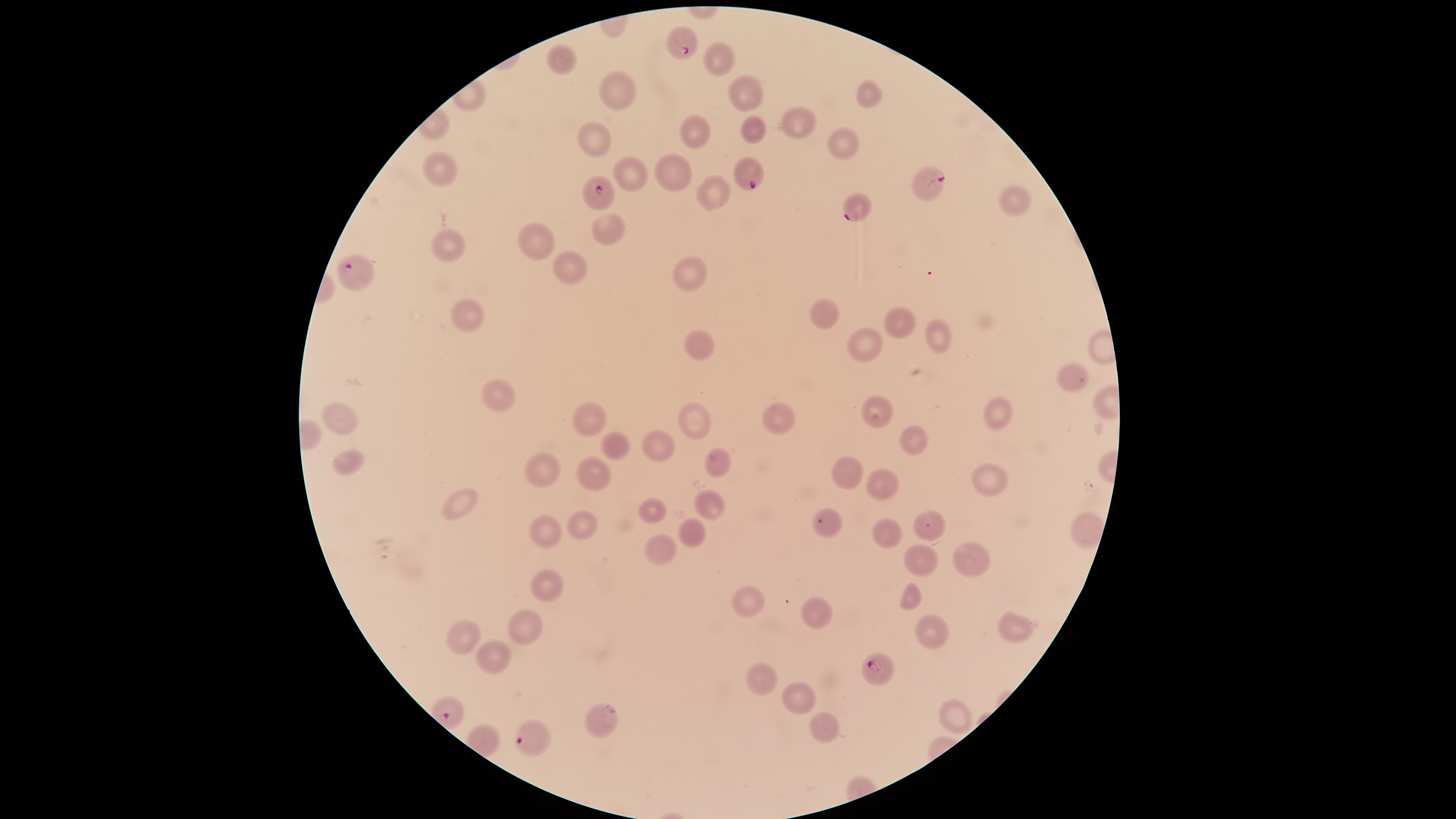

field of view = single
capture = smartphone photograph through the microscope eyepiece
preparation = thin blood smear
uninfected red blood cells = approximate bounding boxes as [left, top, right, bottom] in pixels: [703, 41, 735, 78], [547, 44, 576, 75], [600, 70, 635, 111], [730, 75, 763, 112], [857, 79, 882, 109], [782, 106, 816, 139], [681, 114, 709, 149], [740, 115, 765, 145], [578, 121, 611, 156], [828, 127, 858, 160], [423, 152, 457, 186], [656, 153, 692, 192], [613, 155, 647, 192], [697, 175, 729, 210], [999, 184, 1031, 216], [593, 212, 624, 247], [518, 222, 556, 260], [432, 228, 465, 262], [553, 251, 588, 284], [675, 255, 707, 292], [451, 298, 484, 331], [809, 299, 839, 329], [885, 307, 916, 338], [926, 319, 951, 353], [847, 327, 883, 362], [685, 330, 715, 359], [1058, 361, 1087, 393], [482, 378, 515, 413], [863, 395, 893, 428], [985, 396, 1013, 430], [572, 401, 606, 437], [321, 402, 357, 435], [678, 403, 710, 441], [763, 403, 795, 434], [900, 425, 929, 455], [642, 430, 675, 463], [601, 431, 631, 462], [332, 448, 364, 475], [706, 448, 731, 479], [525, 451, 561, 488], [577, 456, 611, 491], [831, 456, 862, 489], [972, 463, 1008, 498], [866, 468, 898, 500], [442, 487, 479, 520], [695, 490, 725, 520], [638, 497, 667, 525], [567, 511, 597, 540], [913, 511, 945, 542], [1070, 514, 1103, 548], [530, 515, 562, 548], [678, 518, 705, 547], [871, 518, 903, 550], [644, 534, 677, 566], [952, 541, 991, 577], [903, 545, 938, 576], [530, 570, 564, 602], [897, 583, 921, 610], [730, 585, 764, 618], [800, 597, 832, 627], [507, 609, 544, 644], [998, 612, 1032, 642], [915, 614, 948, 649], [445, 619, 482, 655], [476, 640, 511, 676], [746, 662, 777, 696], [781, 682, 816, 714], [939, 699, 972, 733], [585, 704, 619, 739], [808, 711, 840, 744]
stain = Giemsa
image size = 1456×819 pixels
parasitized red blood cells = approximate bounding boxes as [left, top, right, bottom] in pixels: [666, 26, 698, 59], [732, 156, 765, 190], [912, 166, 946, 201], [582, 176, 615, 210], [842, 192, 873, 222], [337, 254, 376, 291], [811, 508, 842, 538], [861, 652, 895, 686], [513, 719, 551, 756]
presence = malaria parasites identified
species = Plasmodium falciparum
visible region = circular